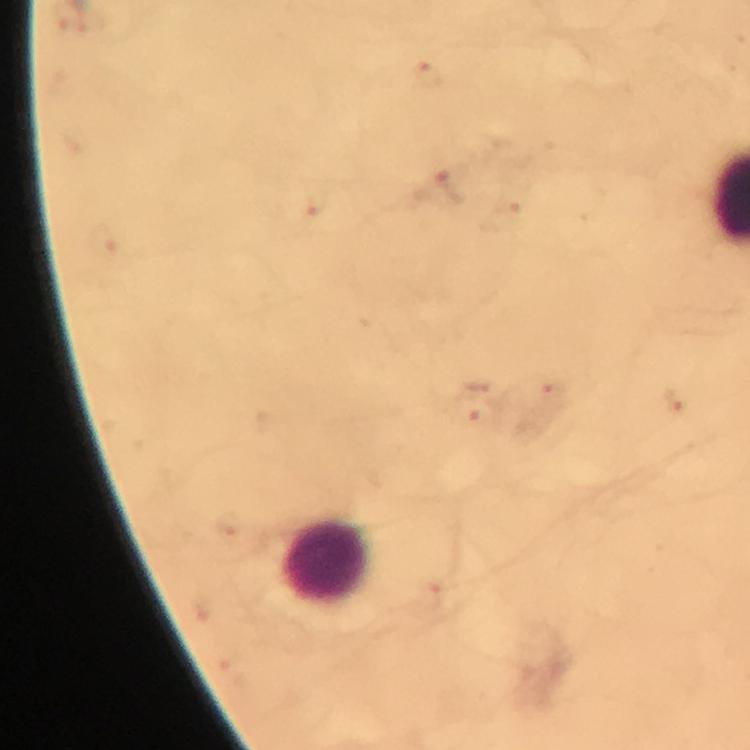
Approximate centers as [x, y] in pixels.
Summary:
  - Leukocyte locations: [327, 564]
  - Plasmodium parasite locations: [428, 72], [449, 185], [319, 203], [672, 404], [469, 410]
  - Cropped from: one field of view
  - Image size: 750×750 pixels
  - Capture: smartphone photograph through a microscope
  - Stain: Giemsa
  - Preparation: thick blood smear
  - Context: from a malaria diagnostic workup
  - Immersion oil: used
  - Magnification: 100x